State which cell type is depicted.
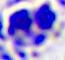
This is a leukocyte.

magnification: 400x
modality: micrograph